State which parasite is depicted.
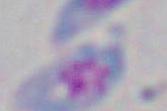
Toxoplasma gondii.

Summary:
  - Magnification: 1000x
  - Modality: photomicrograph